State which cell type is depicted.
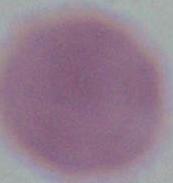

An erythrocyte.

1000x magnification. Micrograph.